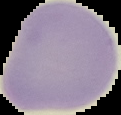
Summary:
  - Image type: segmented cell region on a black background
  - Malaria status: uninfected
  - Image size: 121×115 pixels
  - Preparation: thin blood film